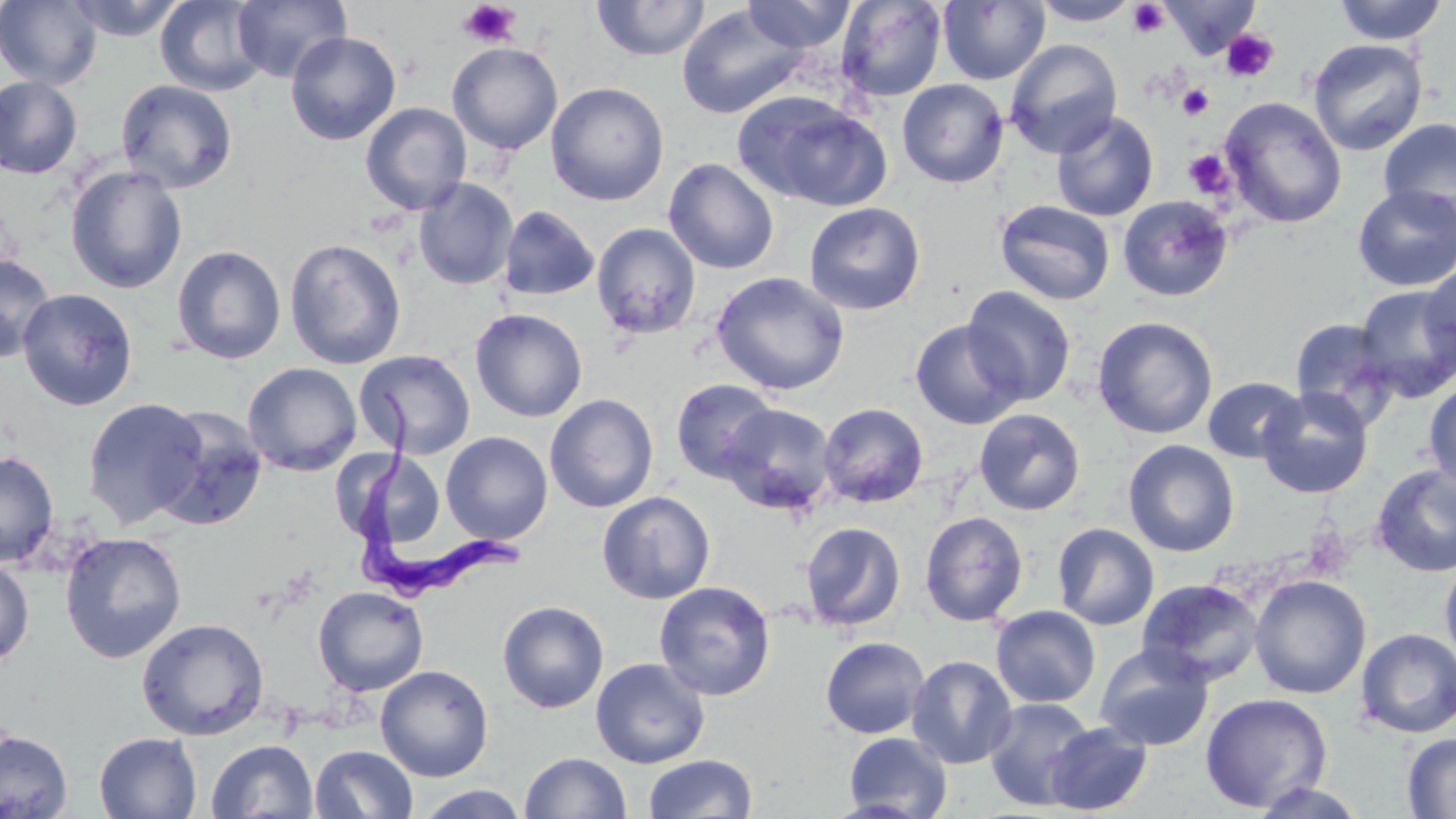

trypanosoma_brucei_locations: 'approximate bounding boxes as [x1, y1, x2, y2] in pixels: [350, 384, 528, 600]'
slide_level_diagnosis: Trypanosoma brucei
image_size: 1456×819 pixels
platelet_locations: 'approximate bounding boxes as [x1, y1, x2, y2] in pixels: [458, 1, 522, 48], [1127, 2, 1169, 38], [1221, 29, 1278, 82], [1178, 84, 1214, 120], [1184, 149, 1232, 198], [1303, 525, 1354, 580]'
stain: May-Grünwald-Giemsa
field_of_view: one of a larger specimen
magnification: 1000x
preparation: thin blood film
modality: optical microscopy
uninfected_red_blood_cell_locations: 'approximate bounding boxes as [x1, y1, x2, y2] in pixels: [0, 0, 102, 90], [64, 0, 187, 41], [155, 0, 269, 96], [231, 0, 351, 83], [742, 0, 856, 53], [836, 0, 947, 102], [1333, 0, 1448, 45], [592, 1, 711, 61], [938, 1, 1050, 85], [1029, 1, 1142, 26], [1159, 1, 1262, 58], [676, 4, 810, 119], [285, 31, 401, 145], [1307, 38, 1428, 156], [1005, 39, 1123, 158], [447, 42, 563, 154], [0, 76, 82, 179], [116, 79, 238, 194], [897, 79, 1009, 188], [545, 81, 669, 206], [734, 92, 891, 211], [1220, 96, 1347, 229], [360, 102, 471, 215], [1051, 112, 1159, 222], [1378, 118, 1456, 228], [664, 158, 779, 274], [65, 165, 187, 294], [413, 178, 518, 290], [1352, 185, 1456, 292], [1117, 195, 1234, 302], [995, 200, 1116, 305], [804, 202, 926, 315], [498, 205, 600, 302], [591, 223, 701, 340], [284, 238, 407, 370], [171, 245, 286, 364], [0, 253, 56, 361], [1419, 266, 1455, 372], [711, 271, 849, 395], [1353, 284, 1456, 402], [962, 286, 1077, 406], [17, 288, 139, 411], [470, 308, 588, 422], [1092, 315, 1218, 439], [1288, 316, 1401, 429], [909, 319, 1026, 430], [354, 349, 476, 459], [242, 362, 363, 476], [1203, 376, 1306, 463], [670, 378, 779, 482], [1424, 379, 1456, 493], [1257, 387, 1374, 499], [544, 393, 659, 513], [82, 397, 208, 528], [818, 402, 929, 508], [719, 403, 837, 515], [152, 406, 268, 531], [974, 408, 1086, 515], [440, 431, 553, 544], [1122, 439, 1240, 557], [0, 450, 59, 567], [335, 452, 458, 545], [1370, 463, 1456, 577], [597, 490, 716, 604], [919, 511, 1029, 627], [801, 522, 906, 631], [1052, 522, 1160, 631], [59, 531, 187, 663], [0, 557, 34, 667], [1440, 558, 1456, 671], [1249, 574, 1371, 699], [1136, 578, 1265, 687], [654, 580, 776, 700], [313, 585, 429, 696], [497, 600, 609, 713], [990, 605, 1101, 708], [136, 617, 270, 740], [1356, 628, 1456, 738], [820, 636, 930, 739], [1094, 644, 1214, 751], [906, 655, 1017, 769], [590, 658, 710, 768], [375, 664, 494, 781], [1200, 692, 1333, 813], [983, 697, 1097, 810], [1043, 721, 1153, 815], [0, 729, 73, 818], [843, 731, 953, 818], [1402, 731, 1456, 818], [94, 732, 202, 818], [206, 739, 318, 819], [309, 745, 418, 819], [520, 752, 631, 818], [642, 753, 757, 818], [1248, 781, 1370, 818], [414, 785, 530, 819]'